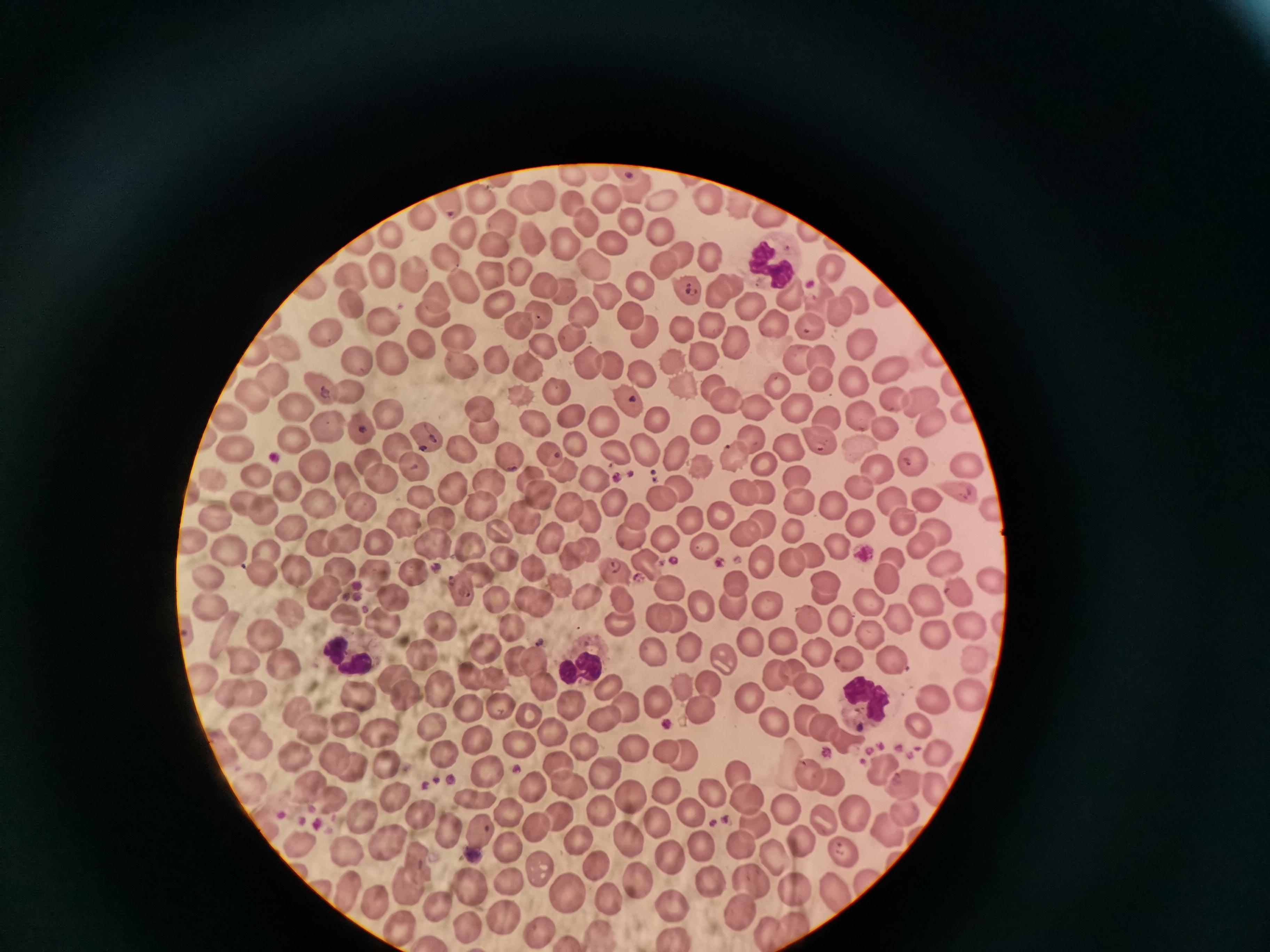

Approximate centers as [x, y] in pixels. Cell locations: [633, 192], [708, 197], [476, 198], [448, 199], [542, 199], [523, 201], [609, 202], [658, 202], [735, 203], [575, 204], [419, 217], [772, 217], [502, 220], [586, 221], [631, 222], [464, 233], [389, 236], [661, 236], [812, 237], [612, 240], [492, 242], [534, 242], [565, 248], [711, 250], [682, 254], [446, 257], [593, 262], [664, 264], [383, 269], [414, 270], [829, 270], [488, 274], [639, 282], [728, 283], [310, 284], [355, 284], [467, 286], [565, 287], [545, 288], [713, 288], [604, 290], [689, 291], [790, 291], [882, 291], [435, 292], [854, 298], [746, 299], [497, 305], [356, 308], [583, 312], [836, 312], [431, 314], [634, 315], [541, 319], [274, 322], [712, 322], [384, 324], [772, 324], [517, 325], [640, 328], [681, 328], [811, 329], [570, 330], [324, 337], [461, 340], [735, 340], [863, 342], [424, 344], [543, 348], [254, 349], [282, 353], [700, 354], [823, 357], [496, 358], [675, 358], [393, 359], [611, 359], [793, 360], [586, 362], [357, 363], [455, 365], [890, 366], [639, 367], [527, 368], [271, 377], [820, 377], [680, 379], [851, 381], [712, 382], [777, 385], [319, 387], [346, 392], [556, 392], [522, 393], [251, 396], [625, 396], [896, 396], [920, 399], [725, 402], [482, 405], [295, 407], [756, 407], [796, 407], [963, 409], [859, 412], [389, 414], [532, 417], [658, 418], [232, 419], [576, 419], [606, 419], [929, 420], [830, 422], [324, 423], [482, 425], [365, 428], [702, 428], [884, 430], [820, 437], [755, 438], [292, 440], [428, 441], [574, 443], [400, 444], [228, 445], [639, 445], [858, 446], [459, 448], [611, 449], [794, 449], [368, 451], [674, 451], [549, 456], [734, 456], [765, 457], [505, 459], [915, 459], [313, 461], [968, 465], [411, 466], [563, 469], [697, 469], [880, 470], [346, 473], [380, 475], [594, 475], [796, 475], [528, 478], [259, 479], [490, 482], [218, 485], [856, 485], [457, 486], [676, 486], [286, 488], [738, 489], [758, 490], [955, 490], [534, 493], [924, 497], [659, 498], [890, 498], [246, 499], [314, 500], [419, 500], [615, 501], [800, 501], [833, 501], [355, 502], [478, 502], [568, 506], [262, 509], [636, 511], [719, 511], [587, 513], [527, 514], [855, 517], [441, 518], [901, 518], [761, 519], [217, 521], [689, 521], [401, 523], [290, 528], [794, 528], [500, 529], [734, 530], [933, 530], [626, 534], [194, 537], [552, 537], [343, 539], [666, 539], [374, 541], [437, 542], [835, 542], [318, 544], [920, 544], [586, 546], [812, 547], [471, 549], [699, 549], [268, 554], [224, 556], [571, 557], [765, 557], [787, 559], [891, 559], [508, 561], [944, 563], [650, 568], [532, 569], [615, 569], [339, 570], [301, 571], [476, 572], [260, 573], [208, 575], [386, 575], [420, 575], [888, 580], [988, 582], [822, 584], [558, 585], [737, 586], [956, 586], [671, 587], [460, 590], [326, 593], [583, 593], [392, 594], [526, 595], [619, 595], [821, 595], [494, 596], [925, 600], [205, 603], [539, 603], [703, 603], [866, 603], [729, 604], [768, 605], [656, 612], [291, 615], [351, 615], [672, 615], [616, 617], [808, 617], [893, 618], [383, 620], [839, 620], [517, 627], [968, 627], [438, 628], [936, 631], [868, 634], [749, 637], [265, 638], [782, 638], [687, 644], [649, 648], [816, 650], [488, 652], [422, 655], [720, 655], [845, 658], [971, 658], [240, 660], [533, 660], [895, 663], [286, 664], [795, 671], [470, 674], [775, 674], [398, 676], [494, 677], [202, 680], [705, 682], [809, 684], [545, 686], [684, 686], [607, 687], [970, 689], [411, 691], [233, 692], [363, 693], [751, 694], [251, 695], [659, 700], [936, 700], [498, 703], [469, 704], [568, 705], [622, 705], [699, 707], [298, 712], [526, 716], [602, 716], [803, 720], [346, 722], [772, 722], [245, 723], [819, 724], [435, 726], [916, 726], [376, 728], [550, 730], [318, 734], [843, 735], [475, 736], [254, 744], [222, 745], [514, 745], [583, 745], [631, 747], [938, 750], [663, 751], [681, 753], [438, 754], [297, 757], [336, 758], [350, 764], [557, 764], [881, 764], [393, 770], [485, 771], [606, 773], [738, 773], [808, 773], [905, 781], [833, 783], [533, 784], [565, 784], [935, 786], [705, 787], [308, 788], [664, 790], [254, 792], [627, 795], [474, 797], [744, 798], [397, 799], [331, 801], [598, 806], [784, 806], [506, 808], [848, 810], [691, 812], [900, 812], [363, 815], [818, 816], [560, 817], [423, 819], [657, 820], [752, 820], [534, 826], [884, 826], [451, 831], [479, 832], [740, 838], [384, 839], [577, 840], [631, 841], [301, 842], [804, 842], [505, 845], [702, 847], [349, 850], [843, 852], [779, 854], [672, 857], [418, 862], [592, 862], [539, 872], [707, 876], [639, 881], [508, 883], [470, 884], [788, 884], [409, 885], [749, 885], [348, 888], [831, 890], [567, 891], [607, 899], [377, 901], [672, 903], [438, 904], [742, 911], [504, 917], [468, 922], [798, 922], [394, 923], [539, 928], [773, 930], [601, 931], [675, 934]. Malaria reading: positive. Thin blood smear. One field from this slide. Image is 1270×952 pixels. Giemsa-stained preparation. Photographed with a smartphone camera at the microscope eyepiece.